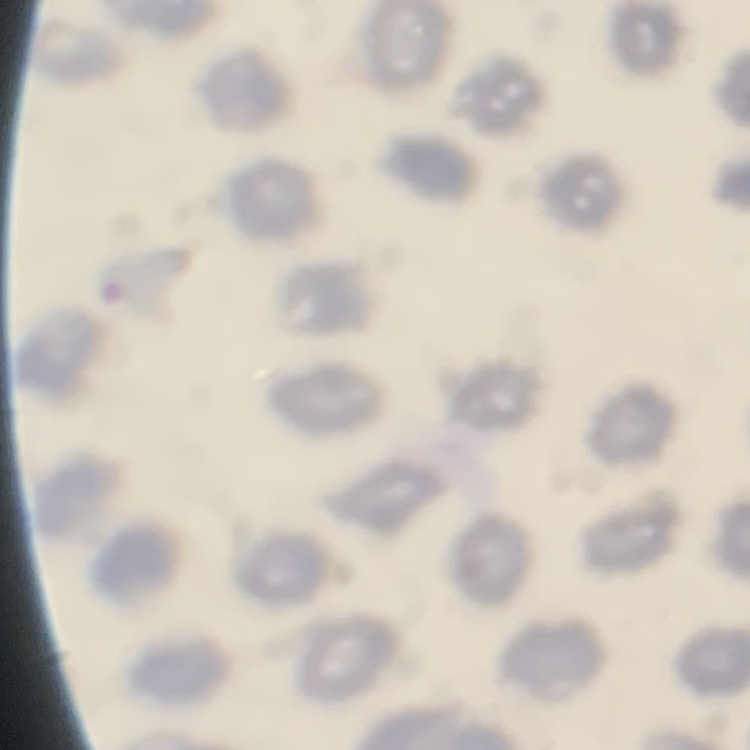
The red blood cells show no rouleaux formation. Field's or Giemsa stain. Square crop of a larger photomicrograph. Thin blood smear.